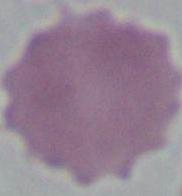
Summary:
  - Modality: micrograph
  - Identification: erythrocyte
  - Magnification: 1000x